Assess the morphology of the erythrocytes.
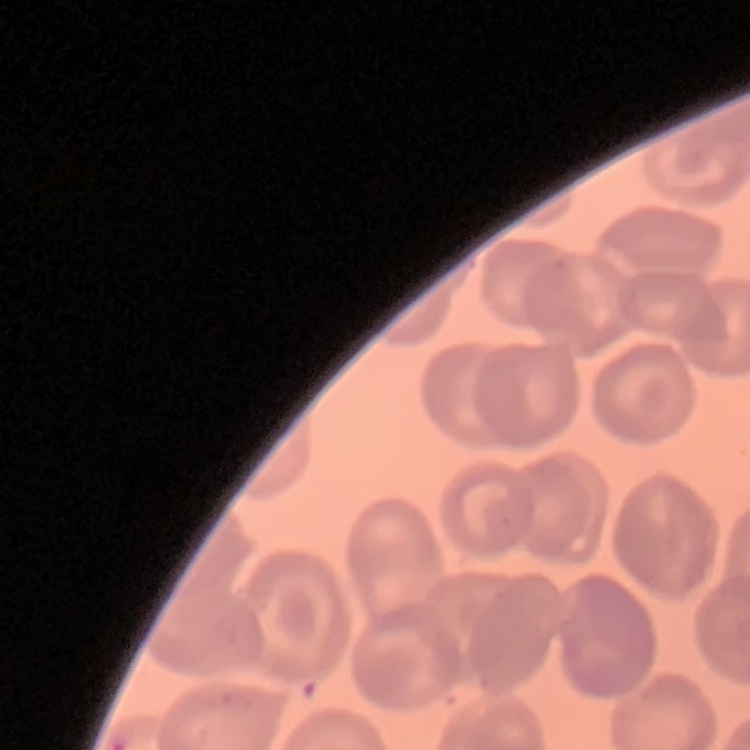

No rouleaux formation.

stain: Field's or Giemsa
preparation: thin blood film
image_type: one tile cut from a larger photomicrograph